Name the cell type shown.
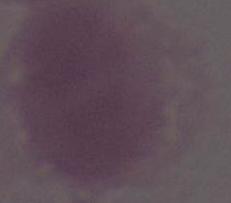
This is an erythrocyte.

modality: micrograph
magnification: 1000x